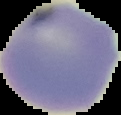

image size = 121×115 pixels
result = negative for malaria parasites
image type = cell region segmented out of the field of view; surrounding area masked to black
preparation = thin blood smear